Report the malaria status of this cell.
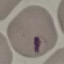
It is parasitized.

image type = automatically extracted cell patch, resized to 64 × 64 pixels
preparation = thin smear
capture = smartphone camera at the microscope eyepiece
stain = Giemsa